Locate every leukocyte (white blood cell).
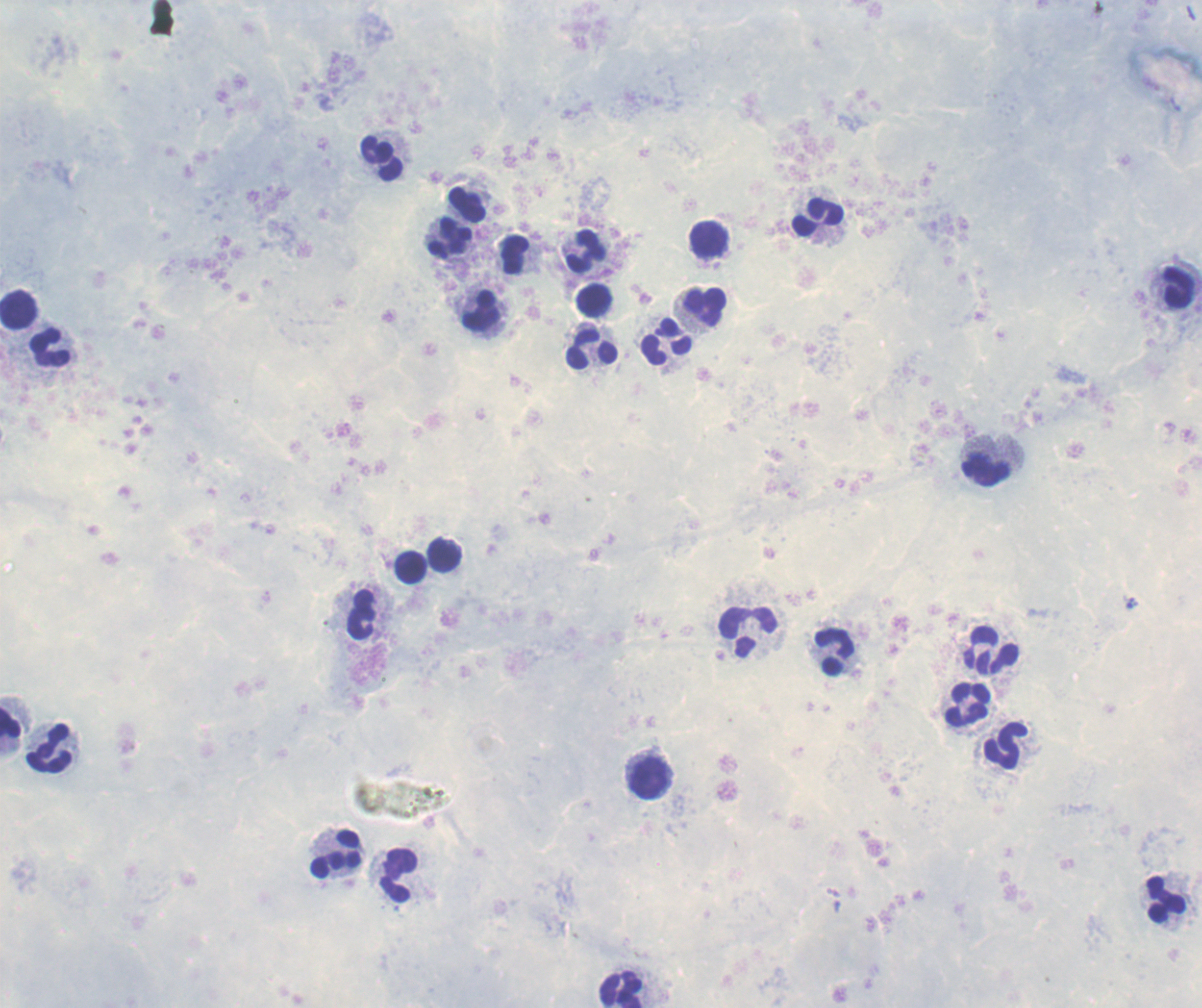

Approximate centers as [x, y] in pixels.
Leukocytes: [382, 158], [468, 205], [818, 217], [449, 238], [709, 241], [587, 250], [514, 254], [1177, 289], [594, 300], [704, 307], [18, 309], [482, 311], [666, 343], [51, 348], [593, 350], [992, 461], [444, 555], [411, 567], [362, 614], [749, 631], [992, 652], [835, 653], [967, 704], [11, 725], [49, 747], [1005, 748], [649, 777], [336, 856], [397, 874], [1166, 901], [622, 989].

preparation = thick blood smear
context = previously used in an actual diagnosis
magnification = 100x
stain = Romanowsky
image size = 1202×1008 pixels
result = no malaria parasites detected
background quality = poor
field of view = one from this slide